Assess this cell for malaria.
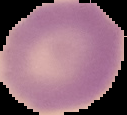

It is uninfected.

image size = 127×115 pixels
image type = segmented cell region with the area outside set to black
preparation = thin blood smear